Give the extent of all Plasmodium falciparum-infected red blood cells.
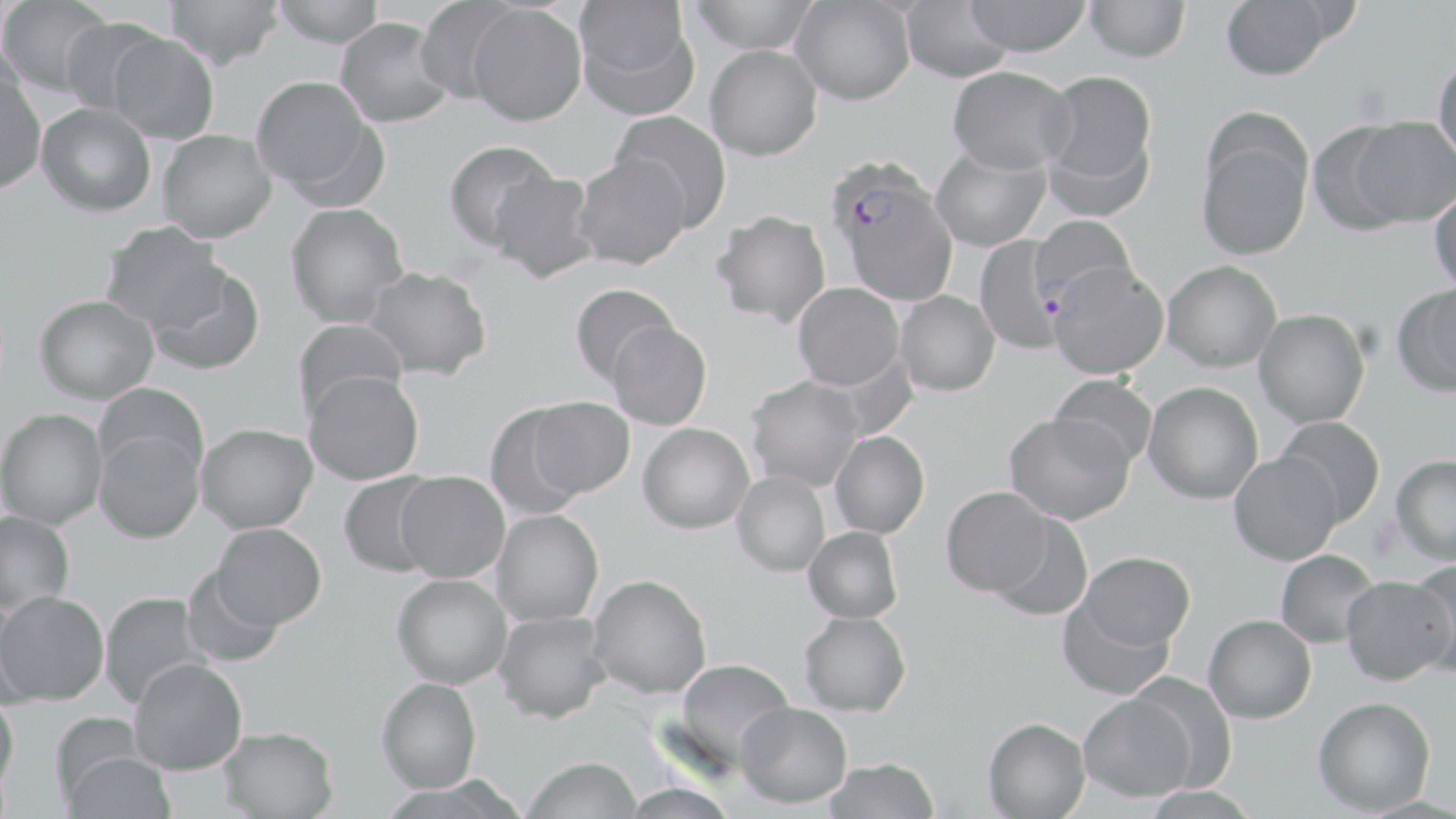

Approximate bounding boxes as (x1, y1, x2, y2) in pixels.
Plasmodium falciparum-infected red blood cells: (827, 163, 957, 305).

slide-level diagnosis = Plasmodium falciparum
modality = optical microscopy
magnification = 1000x
uninfected red blood cell locations = approximate bounding boxes as (x1, y1, x2, y2) in pixels: (0, 0, 113, 96), (166, 0, 283, 69), (272, 0, 384, 47), (415, 0, 521, 103), (690, 0, 820, 53), (963, 0, 1091, 56), (1086, 0, 1190, 62), (1221, 0, 1334, 79), (574, 1, 696, 115), (791, 1, 915, 105), (901, 1, 1014, 82), (467, 4, 586, 125), (60, 17, 168, 118), (336, 18, 453, 127), (108, 31, 219, 144), (705, 45, 822, 161), (1432, 54, 1456, 167), (948, 66, 1076, 174), (0, 70, 46, 194), (1040, 70, 1157, 199), (251, 76, 376, 194), (37, 103, 156, 216), (610, 110, 733, 230), (1349, 117, 1456, 227), (1195, 122, 1312, 261), (1307, 123, 1411, 235), (157, 129, 276, 242), (443, 139, 559, 250), (931, 145, 1051, 251), (574, 152, 691, 269), (489, 171, 599, 283), (1430, 186, 1456, 294), (285, 203, 408, 327), (711, 210, 831, 327), (1030, 215, 1136, 310), (101, 222, 228, 333), (975, 237, 1068, 353), (1162, 259, 1282, 371), (1048, 262, 1169, 379), (148, 265, 266, 375), (363, 266, 493, 380), (793, 282, 904, 390), (1397, 283, 1456, 395), (569, 284, 679, 386), (895, 291, 1000, 396), (34, 294, 159, 404), (1253, 309, 1370, 427), (292, 318, 409, 419), (607, 321, 712, 430), (819, 349, 919, 441), (303, 370, 424, 485), (1050, 375, 1157, 470), (745, 376, 866, 492), (1144, 381, 1263, 503), (94, 382, 209, 479), (527, 396, 634, 498), (483, 403, 588, 519), (0, 408, 107, 529), (1004, 413, 1133, 525), (1275, 416, 1385, 527), (196, 423, 317, 532), (639, 423, 754, 533), (94, 430, 205, 544), (830, 431, 930, 538), (1229, 452, 1342, 565), (1391, 455, 1456, 565), (395, 471, 510, 582), (337, 472, 442, 577), (732, 472, 830, 576), (941, 486, 1052, 596), (491, 509, 604, 626), (0, 511, 75, 616), (988, 515, 1093, 620), (212, 523, 326, 628), (803, 526, 903, 623), (1275, 550, 1380, 647), (1078, 551, 1195, 649), (1410, 559, 1456, 677), (181, 566, 285, 669), (392, 574, 512, 688), (588, 574, 712, 698), (1342, 576, 1454, 685), (0, 591, 109, 704), (99, 592, 208, 708), (0, 595, 36, 707), (1058, 598, 1174, 700), (494, 611, 612, 723), (799, 611, 911, 716), (1204, 614, 1316, 723), (129, 657, 247, 774), (673, 658, 796, 768), (1127, 671, 1238, 792), (377, 677, 482, 792), (0, 692, 19, 798), (1078, 694, 1194, 801), (1313, 696, 1436, 814), (736, 702, 852, 808), (49, 712, 146, 807), (983, 717, 1090, 818), (219, 726, 339, 819), (58, 749, 177, 819), (523, 756, 642, 819), (825, 757, 939, 818), (622, 782, 738, 819)
preparation = thin blood film
stain = May-Grünwald-Giemsa
image size = 1456×819 pixels
field of view = one of a larger specimen